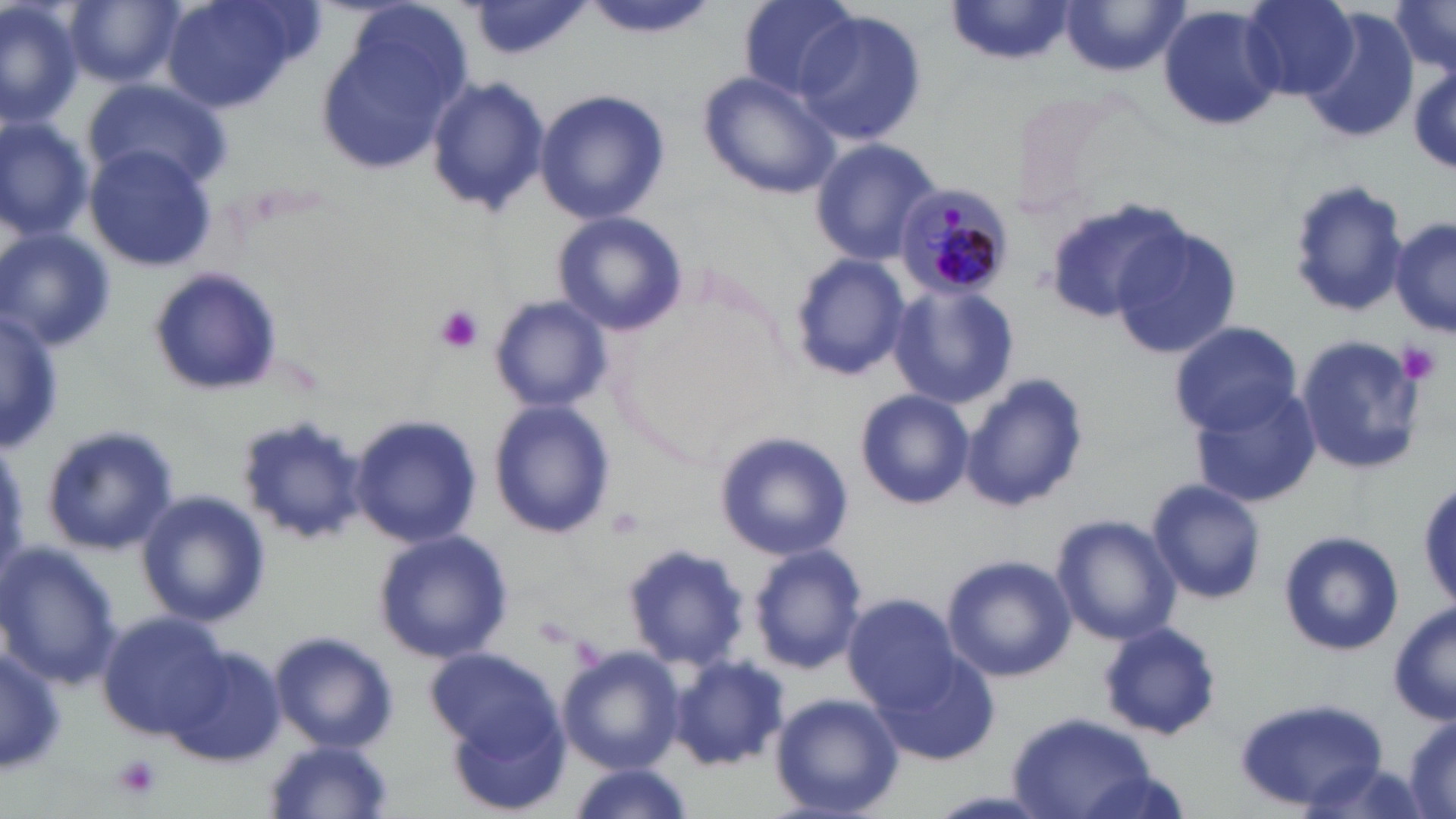

Summary:
  - Coordinate format: approximate bounding boxes as (x1, y1, x2, y2) in pixels
  - Plasmodium malariae-infected red blood cell locations: (896, 184, 1015, 297)
  - Uninfected red blood cell locations: (65, 0, 181, 87), (160, 0, 315, 116), (736, 0, 858, 99), (1243, 0, 1358, 99), (1390, 0, 1456, 74), (2, 1, 82, 130), (588, 2, 708, 41), (947, 2, 1077, 68), (1059, 2, 1185, 77), (469, 3, 590, 62), (1157, 6, 1285, 134), (793, 11, 928, 146), (1300, 11, 1421, 144), (316, 19, 468, 175), (698, 69, 840, 199), (424, 76, 550, 218), (82, 81, 229, 194), (534, 88, 669, 227), (1006, 91, 1138, 212), (0, 117, 93, 241), (809, 136, 942, 266), (84, 145, 218, 271), (1287, 176, 1410, 319), (1043, 196, 1192, 324), (552, 212, 688, 336), (1391, 214, 1455, 341), (1110, 225, 1242, 359), (0, 229, 116, 352), (788, 252, 912, 379), (147, 267, 284, 396), (886, 282, 1019, 410), (487, 293, 613, 414), (0, 309, 60, 452), (1169, 320, 1303, 436), (1290, 333, 1430, 475), (959, 375, 1091, 514), (854, 388, 974, 511), (1190, 390, 1322, 511), (487, 399, 617, 541), (237, 412, 368, 542), (350, 414, 480, 547), (37, 424, 180, 557), (714, 429, 852, 562), (1146, 478, 1268, 605), (138, 491, 269, 626), (1052, 514, 1183, 645), (373, 529, 513, 664), (1278, 531, 1404, 658), (623, 541, 751, 670), (0, 544, 125, 688), (750, 544, 867, 674), (941, 553, 1080, 681), (843, 593, 961, 712), (1389, 605, 1455, 727), (98, 614, 227, 735), (1098, 620, 1223, 741), (270, 631, 398, 752), (870, 641, 998, 769), (1, 643, 64, 777), (558, 645, 686, 773), (170, 648, 286, 768), (425, 648, 558, 756), (669, 655, 788, 770), (768, 692, 905, 818), (1233, 698, 1391, 813), (445, 709, 573, 816), (1009, 712, 1157, 819), (1404, 717, 1455, 816), (262, 741, 397, 819), (563, 763, 694, 819)
  - Platelet locations: (432, 304, 484, 355), (1398, 340, 1443, 385), (113, 755, 163, 802)
  - White blood cell locations: (149, 269, 286, 401), (42, 423, 181, 558)
  - Slide-level diagnosis: Plasmodium malariae
  - Modality: optical microscopy
  - Field of view: one of a larger specimen
  - Image size: 1456×819 pixels
  - Preparation: thin blood film
  - Stain: May-Grünwald-Giemsa
  - Magnification: 1000x